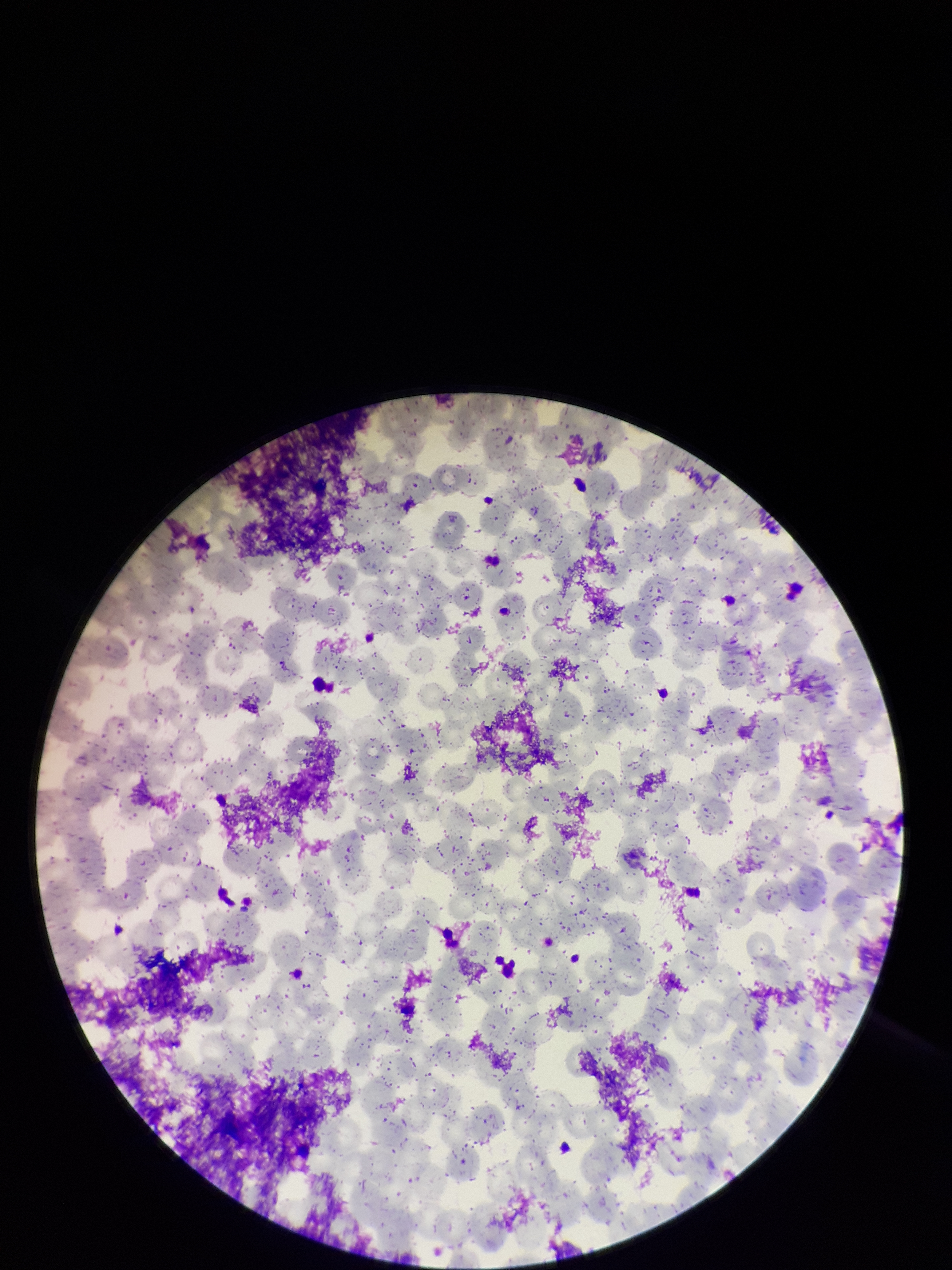
{
  "red_blood_cell_count": 309,
  "parasitized_red_blood_cells": "none identified",
  "field_of_view": "single",
  "capture": "smartphone photograph through the microscope eyepiece",
  "patient_malaria_status": "negative",
  "parasitized_red_blood_cell_count": 0,
  "preparation": "thin smear",
  "stain": "Giemsa",
  "image_size": "952×1270 pixels"
}